Give the extent of all Plasmodium falciparum-infected red blood cells.
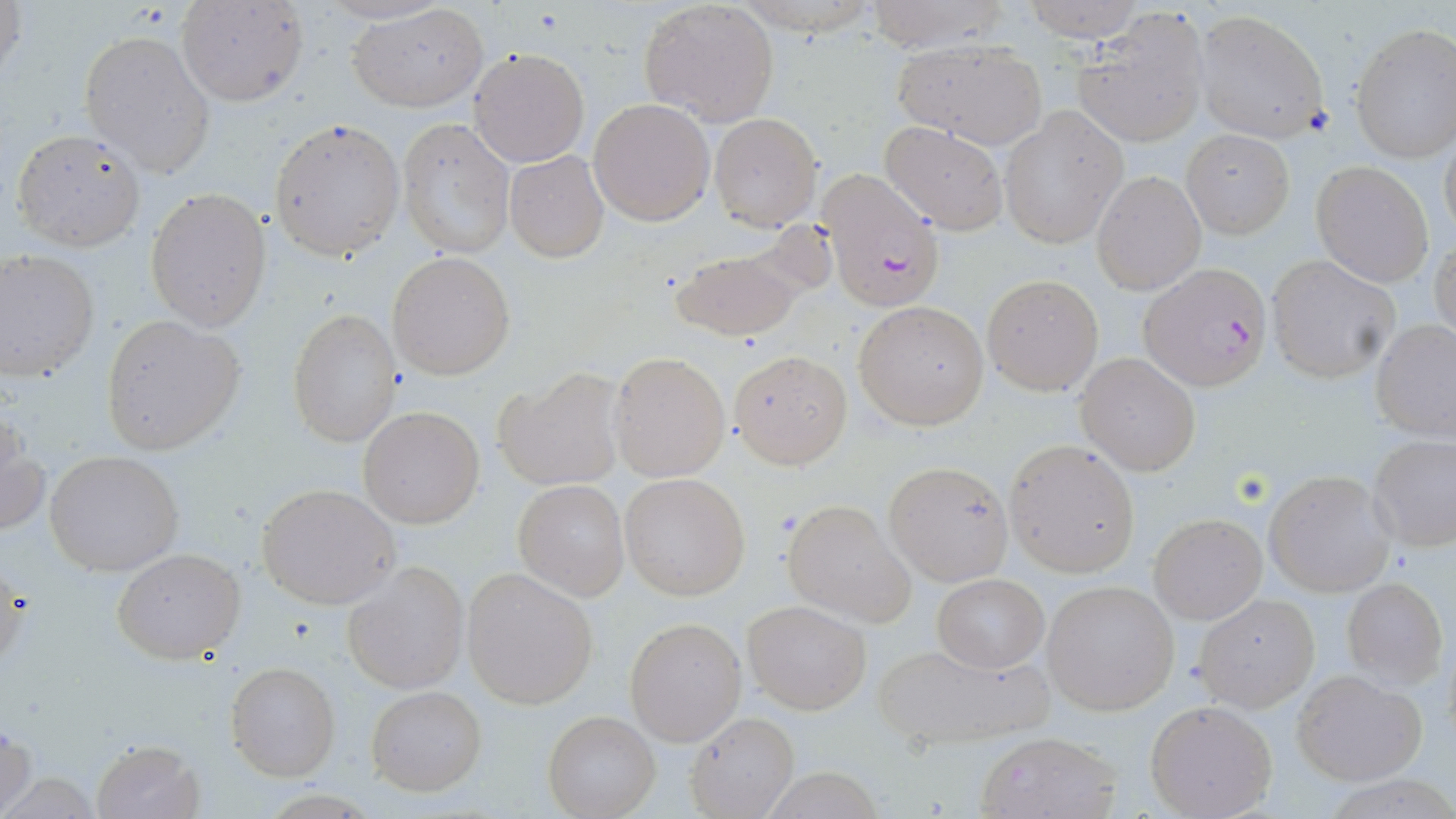

Approximate bounding boxes as (x1, y1, x2, y2) in pixels.
Plasmodium falciparum-infected red blood cells: (816, 168, 944, 310), (1141, 263, 1273, 389).

Summary:
  - Uninfected red blood cell locations: (1, 0, 25, 92), (1021, 0, 1143, 39), (860, 1, 1010, 53), (176, 2, 308, 106), (347, 2, 489, 112), (639, 2, 779, 127), (1074, 9, 1210, 148), (1193, 9, 1330, 143), (1350, 23, 1455, 163), (79, 29, 216, 177), (892, 38, 1048, 147), (469, 47, 591, 167), (589, 97, 715, 225), (999, 107, 1128, 247), (709, 112, 822, 231), (397, 117, 515, 258), (269, 119, 404, 260), (879, 121, 1009, 236), (10, 127, 147, 251), (1183, 128, 1295, 238), (1439, 135, 1455, 244), (504, 150, 610, 262), (1313, 163, 1433, 286), (1092, 170, 1205, 294), (145, 188, 270, 331), (1431, 236, 1456, 348), (668, 245, 811, 342), (0, 250, 99, 383), (387, 252, 515, 379), (1268, 257, 1400, 383), (982, 275, 1104, 395), (852, 300, 989, 430), (286, 309, 401, 446), (98, 315, 244, 453), (1372, 320, 1456, 443), (729, 349, 852, 467), (608, 351, 729, 482), (1074, 351, 1202, 476), (495, 369, 626, 493), (358, 406, 486, 529), (0, 412, 48, 540), (1369, 436, 1456, 551), (1005, 439, 1140, 575), (44, 450, 186, 577), (885, 460, 1013, 587), (1265, 471, 1394, 597), (620, 473, 751, 600), (512, 480, 628, 600), (257, 483, 402, 610), (781, 498, 915, 626), (1149, 513, 1265, 623), (111, 546, 245, 664), (344, 564, 468, 692), (463, 568, 599, 708), (931, 575, 1050, 673), (1342, 577, 1448, 689), (1043, 581, 1178, 714), (1195, 593, 1320, 711), (743, 600, 871, 714), (625, 618, 745, 746), (872, 641, 1052, 749), (226, 660, 341, 782), (1291, 669, 1427, 785), (365, 685, 486, 796), (1144, 701, 1278, 819), (685, 710, 800, 819), (544, 711, 661, 819), (1, 722, 35, 817), (976, 731, 1122, 819), (88, 738, 206, 819)
  - Slide-level diagnosis: Plasmodium falciparum
  - Field of view: one of a larger specimen
  - Stain: May-Grünwald-Giemsa
  - Image size: 1456×819 pixels
  - Preparation: thin blood film
  - Modality: light microscopy
  - Magnification: 1000x